Classify this cell by malaria status.
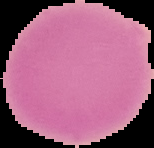

Uninfected.

Image is 154×148 pixels. From a thin blood film. The area outside the segmented cell region is set to black.